Assess this cell for malaria.
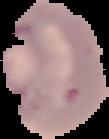

Uninfected.

Summary:
  - Image type: segmented cell region with the area outside set to black
  - Image size: 109×139 pixels
  - Preparation: thin blood smear